Assess for malaria.
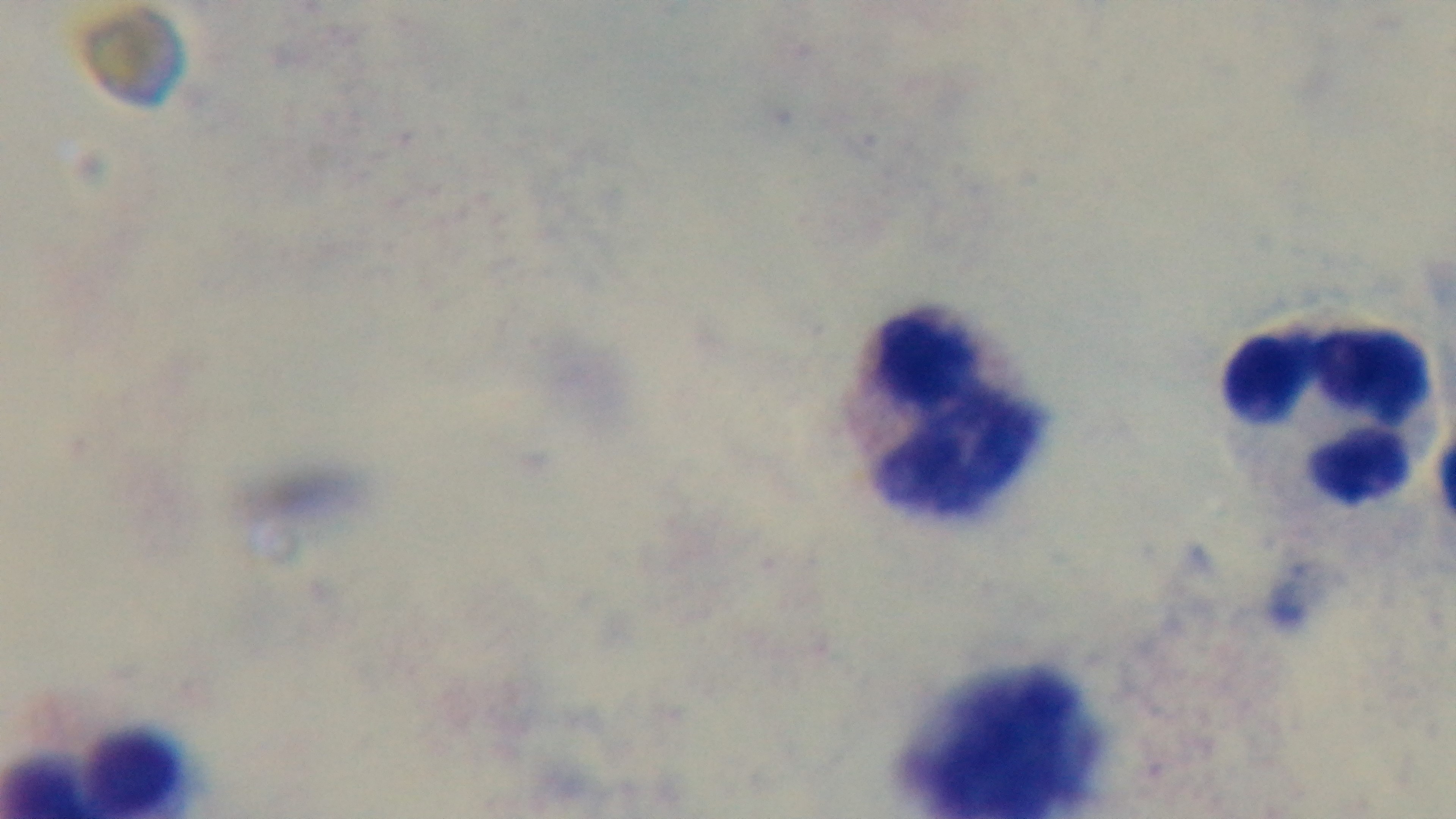
It is uninfected.

capture = mounted 4K digital camera
preparation = thick blood film
stain = Giemsa
modality = light microscopy
objective = 100x oil immersion
field of view = one from the slide